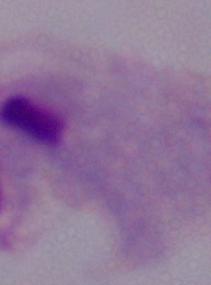
Summary:
  - Identification: trichomonad
  - Modality: photomicrograph
  - Magnification: 1000x